Classify this cell by malaria status.
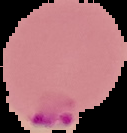

It is parasitized.

image type = segmented cell region on a black background
preparation = thin blood film
image size = 127×133 pixels